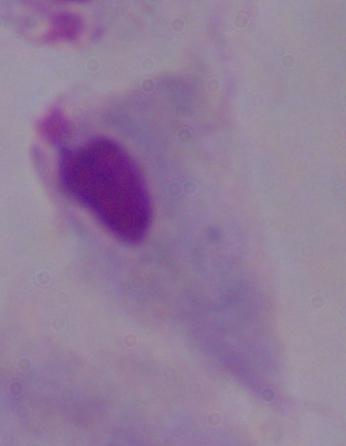 A trichomonad is seen. 1000x magnification. Photomicrograph.